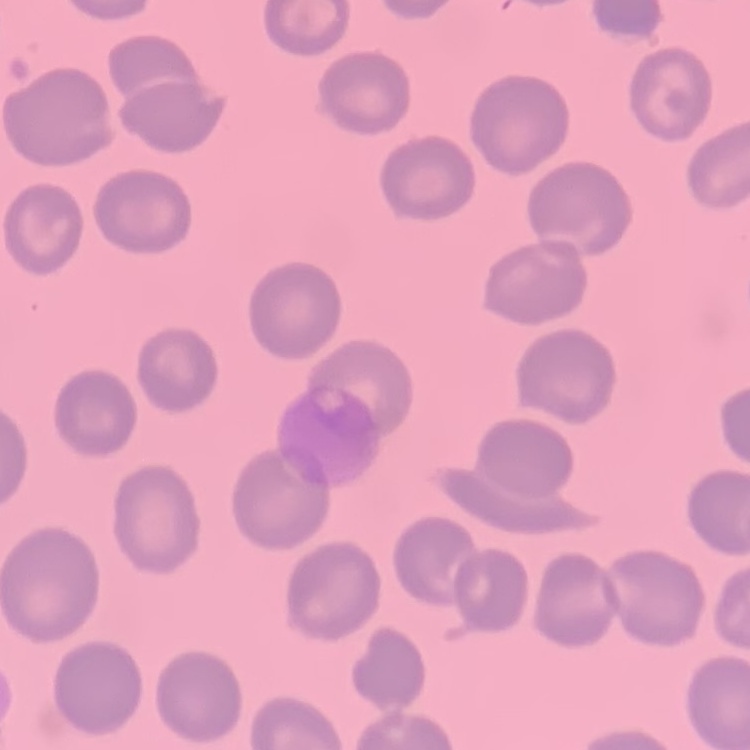 The erythrocytes show no rouleaux formation. Field's or Giemsa stain. Thin blood film. One tile cut from a larger photomicrograph.